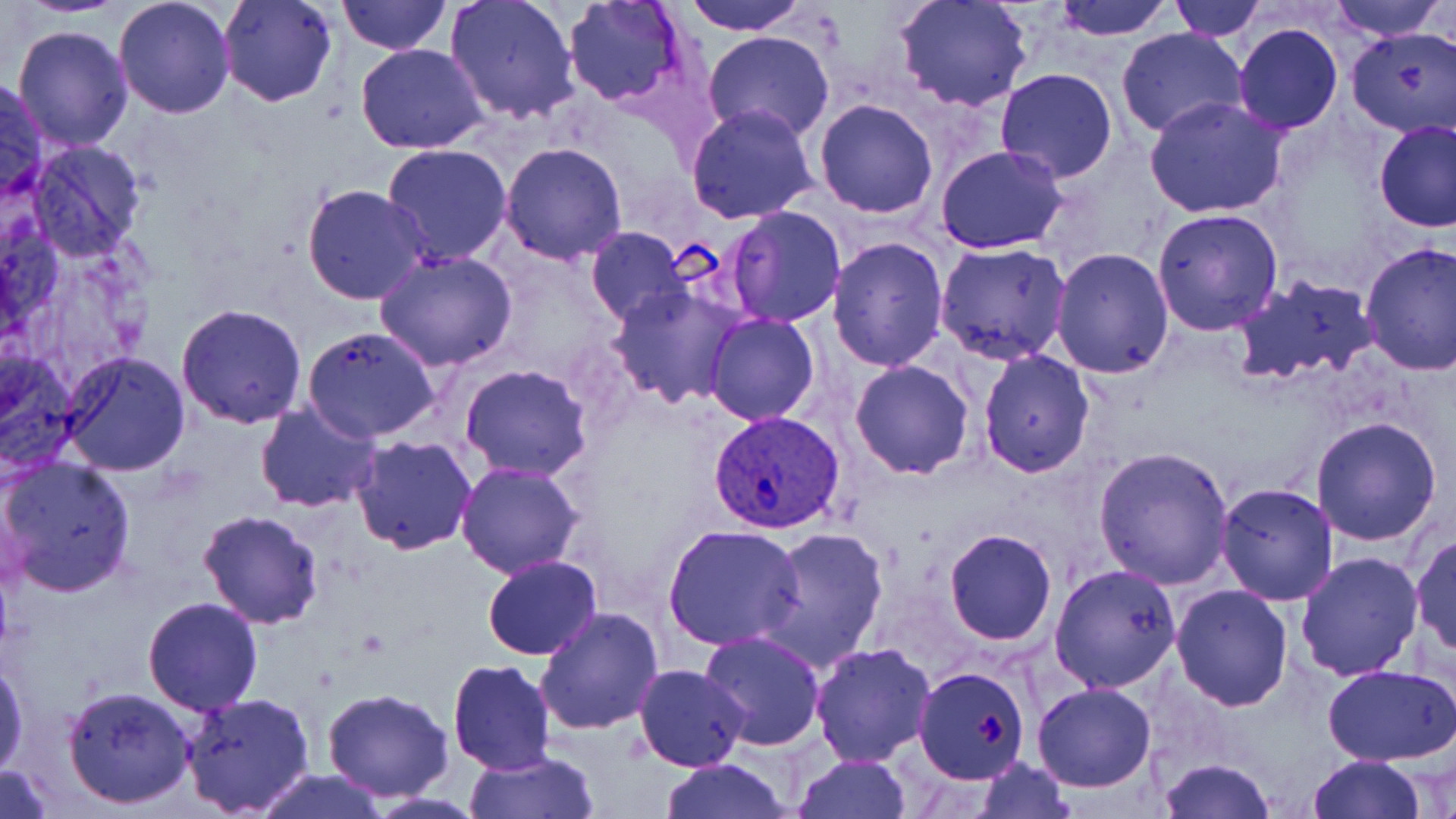
Summary:
  - Coordinate format: approximate bounding boxes as (x1, y1, x2, y2) in pixels
  - Plasmodium vivax-infected red blood cell locations: (707, 409, 846, 536)
  - Uninfected red blood cell locations: (15, 0, 133, 17), (113, 0, 236, 119), (217, 0, 339, 107), (337, 0, 449, 55), (445, 0, 581, 125), (679, 0, 809, 36), (892, 0, 1035, 114), (1051, 0, 1175, 41), (1167, 0, 1268, 41), (1325, 0, 1449, 42), (562, 1, 691, 111), (12, 23, 134, 152), (1232, 23, 1343, 134), (1116, 27, 1247, 137), (1346, 27, 1456, 137), (703, 30, 836, 144), (355, 42, 490, 155), (994, 69, 1120, 184), (0, 76, 48, 208), (1144, 96, 1288, 218), (814, 98, 939, 219), (686, 104, 819, 224), (1375, 121, 1456, 233), (25, 142, 148, 264), (500, 142, 628, 264), (381, 143, 512, 265), (936, 146, 1068, 254), (301, 184, 431, 305), (725, 206, 847, 327), (1152, 207, 1284, 336), (585, 227, 689, 326), (826, 237, 949, 373), (934, 242, 1073, 366), (1359, 242, 1456, 379), (1050, 247, 1177, 378), (374, 251, 518, 371), (1230, 273, 1379, 389), (605, 283, 748, 409), (177, 303, 308, 426), (702, 312, 820, 425), (301, 327, 443, 442), (0, 349, 81, 475), (61, 350, 193, 477), (978, 350, 1095, 478), (849, 360, 976, 478), (460, 364, 592, 481), (254, 400, 382, 514), (1310, 415, 1442, 545), (350, 435, 477, 554), (1093, 448, 1235, 589), (1, 455, 137, 598), (455, 463, 584, 580), (1215, 482, 1340, 605), (198, 509, 325, 628), (662, 524, 807, 650), (758, 526, 889, 670), (943, 530, 1057, 646), (1410, 532, 1456, 659), (1294, 551, 1424, 683), (482, 555, 602, 659), (1048, 563, 1182, 692), (1170, 584, 1293, 711), (142, 596, 265, 715), (535, 606, 664, 735), (697, 631, 825, 752), (808, 642, 936, 767), (447, 657, 555, 774), (0, 658, 27, 779), (633, 663, 749, 771), (1323, 664, 1456, 764), (914, 665, 1032, 784), (1032, 681, 1157, 793), (63, 684, 196, 809), (321, 687, 455, 801), (179, 690, 317, 816), (463, 748, 601, 819), (791, 754, 911, 818), (1307, 754, 1426, 819), (1156, 757, 1275, 819), (657, 758, 795, 818), (974, 759, 1074, 817), (0, 764, 53, 817), (248, 771, 391, 819)
  - Slide-level diagnosis: Plasmodium vivax
  - Stain: May-Grünwald-Giemsa
  - Preparation: thin blood film
  - Field of view: single
  - Magnification: 1000x
  - Modality: optical microscopy
  - Image size: 1456×819 pixels